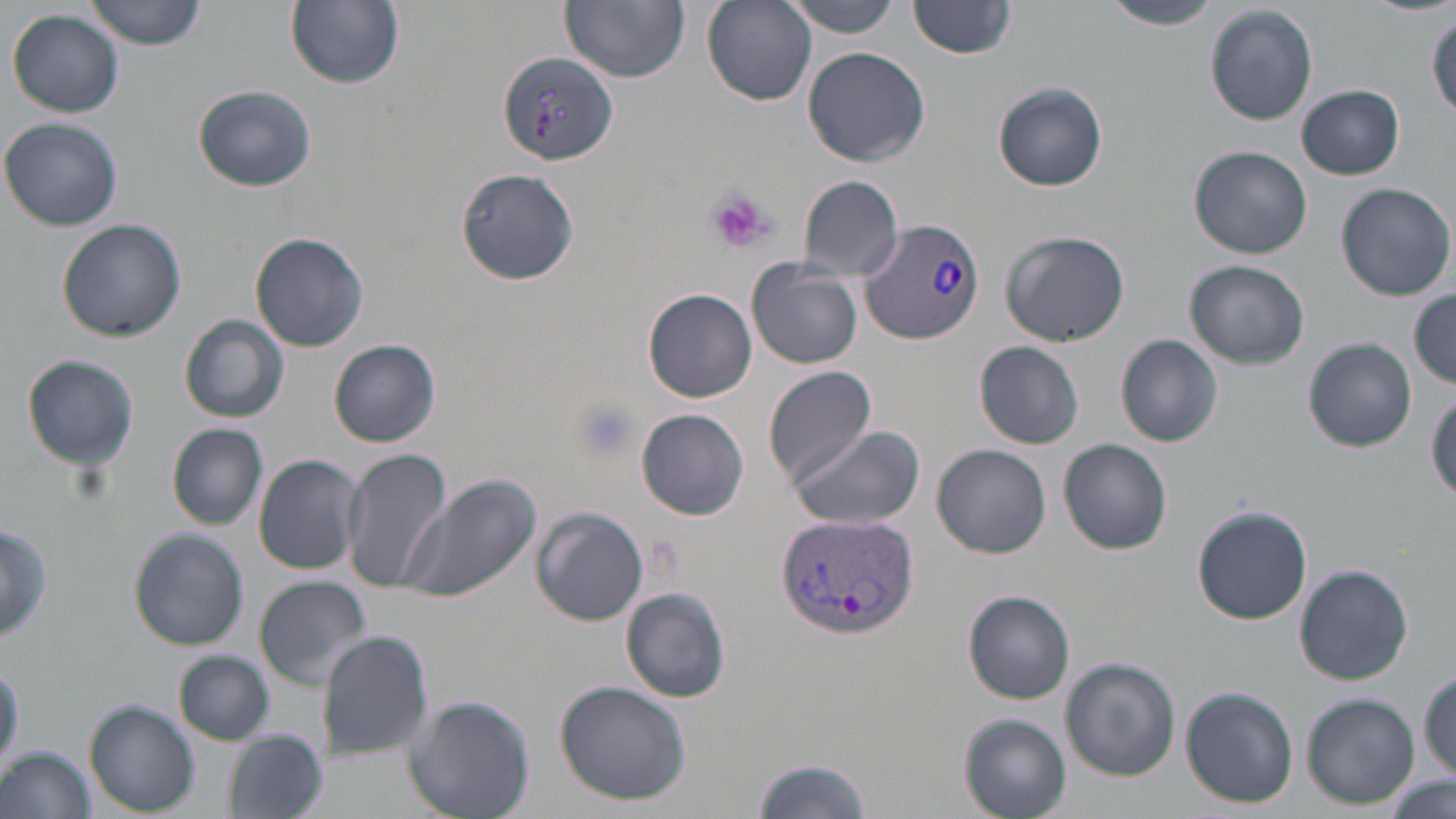
Summary:
  - Coordinate format: approximate bounding boxes as (x1, y1, x2, y2) in pixels
  - Uninfected red blood cell locations: (85, 0, 208, 50), (288, 0, 404, 89), (560, 0, 690, 84), (783, 0, 906, 37), (701, 1, 817, 106), (910, 1, 1018, 58), (1100, 1, 1220, 31), (1205, 5, 1318, 125), (7, 9, 125, 117), (1429, 11, 1456, 120), (802, 46, 931, 169), (995, 82, 1108, 191), (194, 84, 316, 192), (1297, 84, 1405, 180), (1, 117, 125, 232), (1189, 145, 1312, 258), (454, 168, 580, 286), (797, 175, 904, 279), (1336, 181, 1455, 301), (56, 217, 186, 341), (1000, 229, 1130, 348), (251, 232, 372, 353), (1185, 260, 1309, 368), (747, 263, 862, 370), (643, 288, 758, 403), (1409, 289, 1456, 388), (180, 315, 290, 424), (1116, 334, 1224, 446), (1304, 338, 1417, 451), (330, 339, 441, 448), (976, 341, 1086, 448), (20, 352, 139, 469), (763, 367, 879, 486), (1427, 389, 1456, 502), (637, 408, 750, 521), (167, 423, 267, 528), (783, 424, 925, 530), (1059, 438, 1172, 555), (933, 444, 1051, 558), (340, 446, 456, 592), (253, 454, 365, 575), (399, 473, 543, 603), (1191, 505, 1312, 624), (531, 506, 649, 626), (1, 518, 54, 646), (128, 529, 249, 651), (1293, 565, 1414, 685), (254, 575, 373, 689), (621, 588, 730, 703), (964, 591, 1075, 704), (318, 631, 433, 756), (174, 650, 275, 745), (1061, 657, 1179, 779), (1419, 668, 1455, 779), (554, 680, 693, 807), (1180, 686, 1298, 808), (1300, 692, 1419, 807), (404, 694, 535, 819), (85, 701, 199, 816), (959, 715, 1069, 818), (226, 731, 326, 819), (1, 746, 96, 819), (753, 753, 875, 819), (1384, 776, 1455, 819)
  - Plasmodium vivax-infected red blood cell locations: (498, 52, 621, 164), (857, 219, 988, 345), (775, 513, 919, 642)
  - Platelet locations: (704, 187, 775, 254), (567, 396, 640, 462)
  - Slide-level diagnosis: Plasmodium vivax
  - Preparation: thin blood film
  - Stain: May-Grünwald-Giemsa
  - Magnification: 1000x
  - Modality: light microscopy
  - Image size: 1456×819 pixels
  - Field of view: one of a larger specimen